Report the malaria status of this cell.
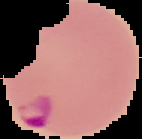

Parasitized.

Summary:
  - Image type: cell region segmented out of the field of view; surrounding area masked to black
  - Image size: 142×139 pixels
  - Preparation: thin blood smear